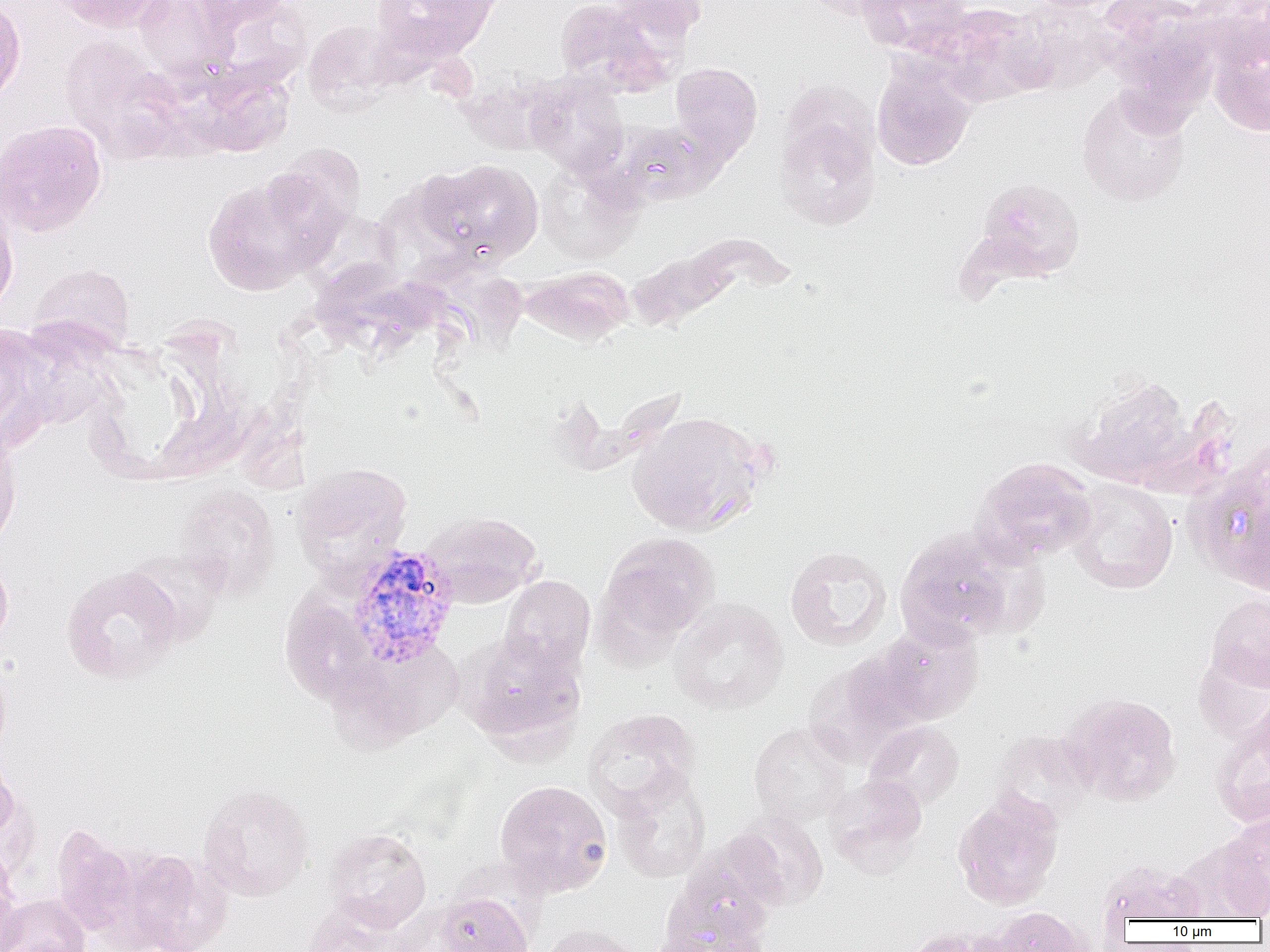

Approximate bounding boxes as [x1, y1, x2, y2] in pixels. Uninfected red blood cell locations: [51, 0, 172, 34], [133, 0, 237, 80], [195, 0, 291, 33], [370, 0, 495, 61], [554, 0, 670, 95], [607, 0, 708, 44], [801, 0, 897, 20], [855, 0, 972, 55], [1095, 0, 1220, 93], [1188, 0, 1270, 70], [0, 1, 26, 107], [1010, 2, 1119, 93], [931, 3, 1051, 107], [303, 20, 401, 114], [1207, 30, 1270, 136], [60, 36, 189, 165], [871, 61, 976, 171], [671, 62, 763, 162], [457, 74, 557, 155], [525, 74, 629, 178], [1076, 85, 1192, 207], [775, 116, 880, 229], [0, 119, 107, 237], [614, 119, 725, 206], [262, 143, 367, 249], [421, 158, 544, 265], [535, 161, 642, 262], [202, 176, 331, 295], [961, 192, 1091, 301], [0, 198, 18, 316], [624, 249, 734, 331], [28, 263, 136, 356], [519, 266, 634, 345], [0, 323, 52, 445], [1071, 372, 1198, 491], [627, 410, 768, 536], [0, 434, 21, 551], [1187, 453, 1270, 595], [972, 457, 1097, 564], [292, 462, 413, 582], [1066, 478, 1178, 594], [175, 485, 281, 602], [421, 510, 544, 608], [894, 527, 1027, 648], [598, 532, 720, 643], [785, 546, 892, 651], [0, 551, 13, 652], [61, 565, 184, 684], [499, 575, 596, 675], [1206, 594, 1270, 692], [669, 598, 789, 715], [870, 623, 984, 726], [460, 633, 586, 752], [328, 640, 462, 750], [1192, 649, 1270, 743], [805, 652, 922, 765], [1252, 687, 1270, 781], [1064, 692, 1182, 805], [583, 708, 700, 818], [864, 720, 964, 811], [1210, 720, 1270, 828], [750, 722, 851, 826], [989, 729, 1097, 829], [0, 753, 22, 848], [611, 772, 711, 883], [825, 773, 928, 874], [494, 780, 612, 897], [197, 784, 316, 900], [952, 790, 1064, 910], [726, 811, 829, 910], [1216, 811, 1270, 917], [51, 824, 140, 936], [323, 827, 432, 933], [1174, 835, 1267, 922], [667, 845, 779, 948], [118, 849, 231, 951], [0, 851, 23, 952], [1095, 859, 1209, 924], [436, 890, 534, 952], [1, 893, 91, 952], [388, 902, 481, 952], [654, 902, 774, 952], [302, 904, 408, 952], [986, 906, 1091, 952], [538, 924, 644, 952], [902, 928, 998, 952]. Plasmodium vivax-infected red blood cell locations: [345, 545, 460, 668]. Slide-level diagnosis: Plasmodium vivax. Light microscopy. Image is 1270×952 pixels. 1000x magnification. Single field of view. Thin blood smear.